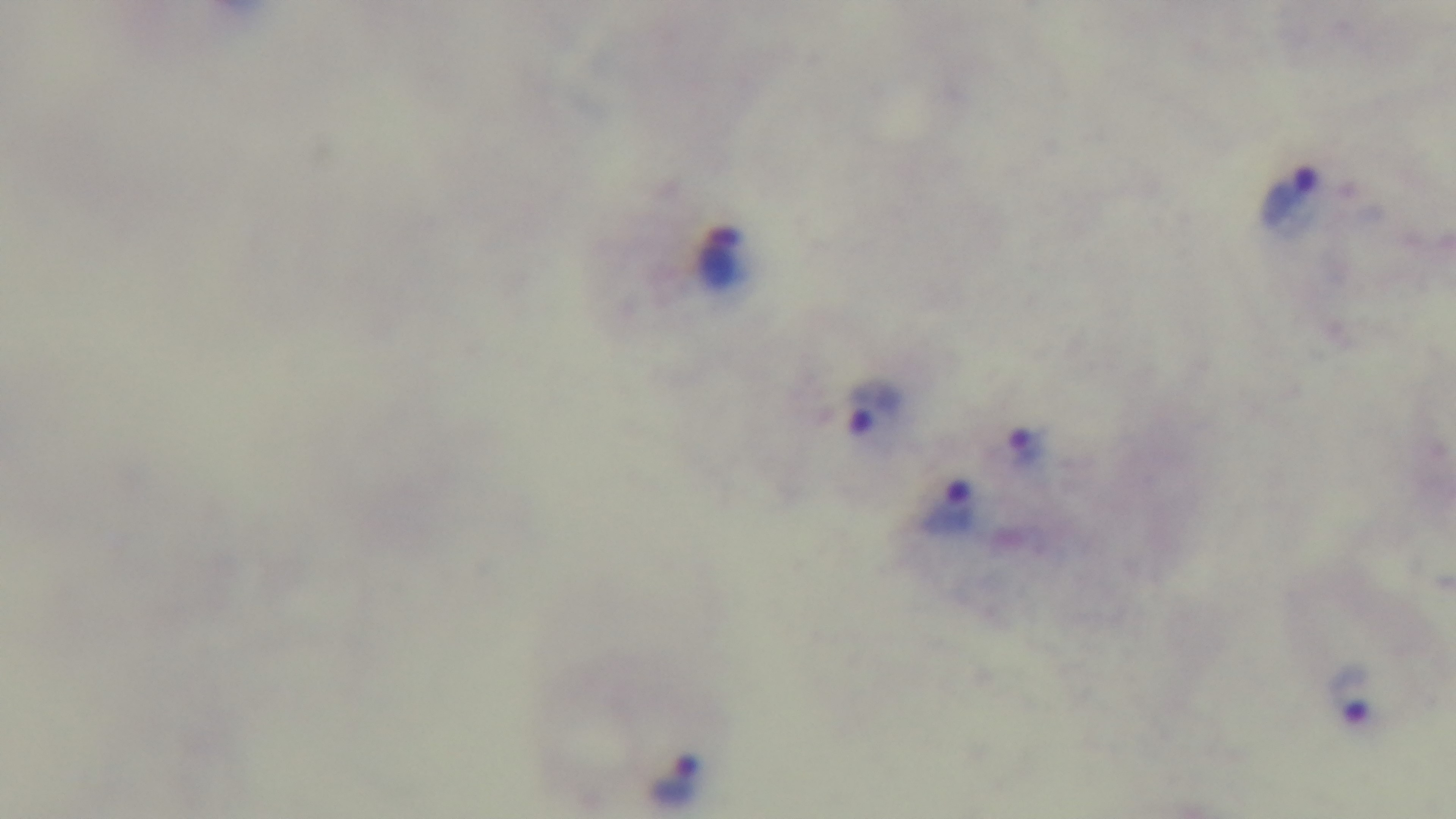
preparation = thick smear
stain = Giemsa
malaria status = positive
field of view = single
modality = light microscopy
objective = 100x oil immersion
capture = mounted 4K digital camera